Assess this cell for malaria.
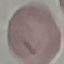
Uninfected.

Photographed with a smartphone camera at the microscope eyepiece. Giemsa stain. Thin blood film. Cell patch, automatically extracted from a larger field of view and resized to 64 × 64 pixels.